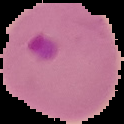
image size = 124×124 pixels
preparation = thin blood smear
result = malaria parasites detected
image type = cell region segmented out of the field of view; surrounding area masked to black